State which parasite is depicted.
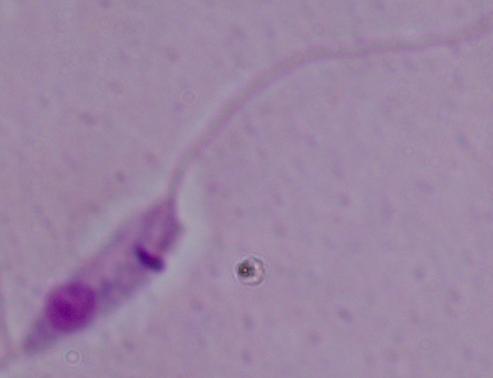

Leishmania.

Summary:
  - Modality: micrograph
  - Magnification: 1000x